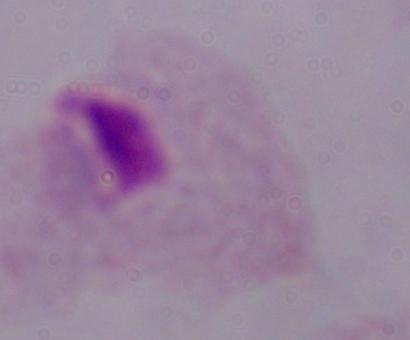

Photomicrograph. A trichomonad is shown. 1000x magnification.